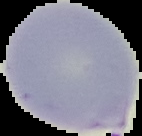

image type = cell region segmented out of the field of view; surrounding area masked to black
preparation = thin blood film
malaria status = parasitized
image size = 142×136 pixels